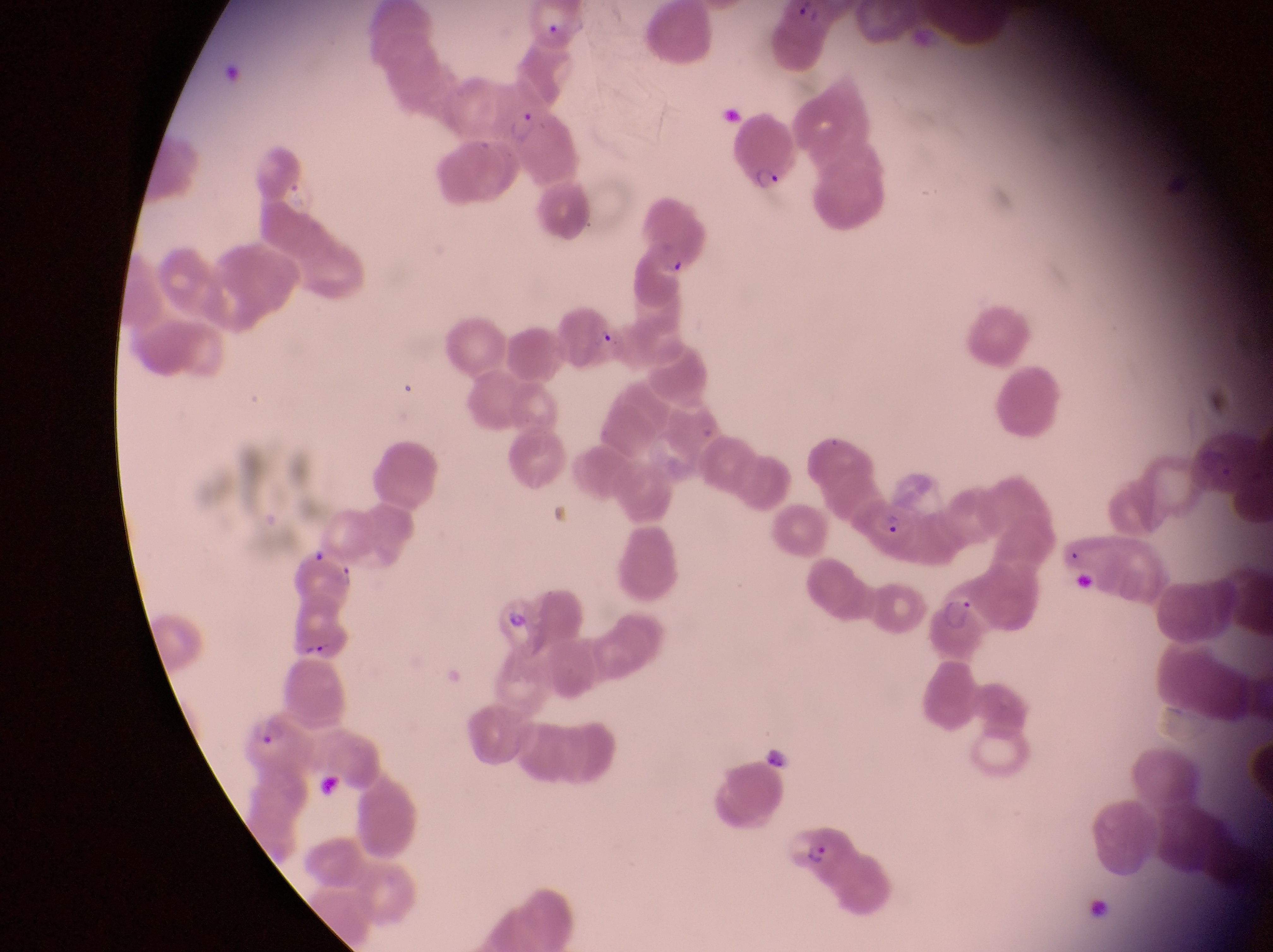
Approximate bounding boxes as (left, top, right, bottom) in pixels.
Summary:
  - Parasitised red blood cell locations: (729, 104, 794, 191), (505, 107, 545, 150), (626, 192, 709, 279), (858, 495, 927, 558), (933, 586, 988, 666), (491, 589, 561, 659), (245, 707, 315, 779), (784, 826, 847, 873)
  - Field of view: single
  - Capture: smartphone photograph through the eyepiece of an Olympus CX-23 microscope
  - Country: Uganda
  - Preparation: thin blood film
  - Image size: 1273×952 pixels
  - Magnification: 1000x